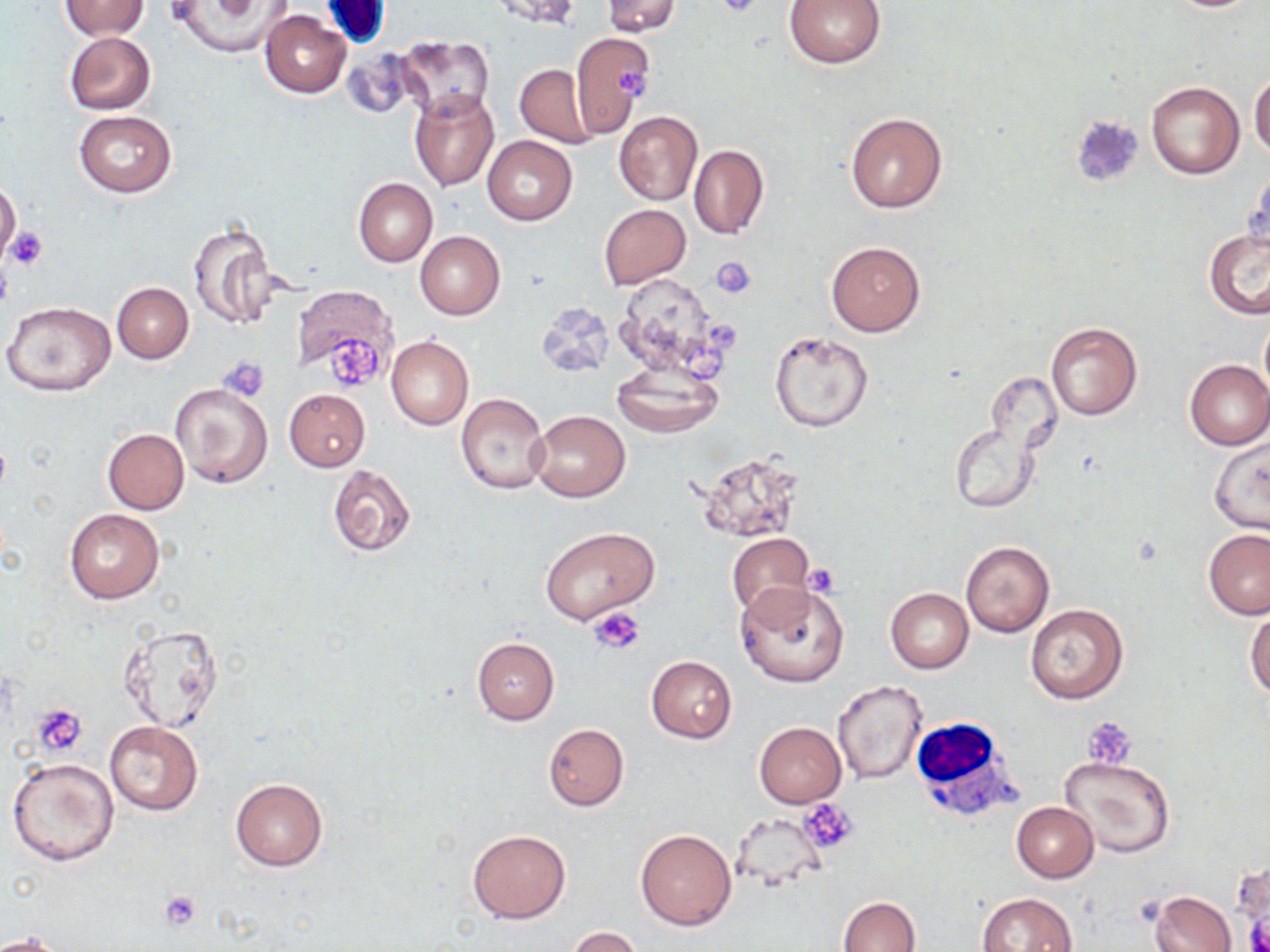

Summary:
  - Coordinate format: approximate bounding boxes as (x1,y1)-(x2,y2) corner pairs in pixels
  - Uninfected red blood cell locations: (485,0)-(583,28), (601,0)-(681,37), (783,0)-(887,68), (59,1)-(150,41), (169,1)-(293,57), (1165,1)-(1260,13), (260,9)-(351,98), (569,31)-(655,137), (63,32)-(156,115), (391,36)-(495,120), (514,64)-(597,147), (1249,72)-(1270,162), (1146,81)-(1244,180), (409,89)-(499,190), (73,111)-(176,197), (613,111)-(703,206), (846,112)-(947,214), (482,136)-(577,225), (688,145)-(768,241), (1246,168)-(1269,256), (353,178)-(438,266), (0,181)-(21,262), (599,204)-(690,288), (187,223)-(284,330), (1202,228)-(1270,319), (415,231)-(505,320), (826,241)-(925,337), (615,274)-(724,379), (112,282)-(194,363), (292,284)-(399,384), (3,302)-(114,396), (535,302)-(613,378), (1260,318)-(1270,395), (1045,321)-(1143,420), (770,330)-(873,433), (386,335)-(473,430), (1183,359)-(1270,450), (612,365)-(722,437), (169,382)-(272,489), (284,389)-(370,472), (455,393)-(550,496), (528,411)-(630,502), (949,421)-(1045,514), (102,429)-(189,515), (1209,439)-(1269,533), (696,451)-(803,542), (327,465)-(417,558), (64,509)-(163,604), (541,526)-(659,625), (1203,528)-(1270,620), (726,531)-(812,621), (960,541)-(1055,638), (736,581)-(849,689), (885,588)-(974,673), (1025,604)-(1128,704), (1246,610)-(1270,700), (118,626)-(226,732), (471,637)-(559,725), (646,656)-(737,743), (832,680)-(929,786), (104,720)-(203,816), (754,722)-(845,808), (543,723)-(629,810), (1059,754)-(1175,857), (8,759)-(119,866), (230,778)-(328,872), (1012,802)-(1098,882), (466,829)-(569,924), (635,830)-(736,930), (1150,890)-(1236,952), (978,891)-(1077,952), (836,897)-(920,952), (568,926)-(645,952), (2,931)-(66,952)
  - White blood cell locations: (910,715)-(1019,822)
  - Platelet locations: (714,0)-(770,19), (616,67)-(652,99), (5,226)-(48,270), (0,253)-(13,311), (711,257)-(757,299), (326,333)-(385,390), (219,356)-(269,402), (803,566)-(839,597), (588,607)-(645,655), (33,703)-(88,758), (1084,716)-(1137,768), (802,799)-(860,853), (159,890)-(202,932), (1246,914)-(1269,952)
  - Slide-level diagnosis: no evidence of blood parasites
  - Preparation: thin blood film
  - Field of view: single
  - Modality: light microscopy
  - Stain: May-Grünwald-Giemsa
  - Magnification: 1000x
  - Image size: 1270×952 pixels